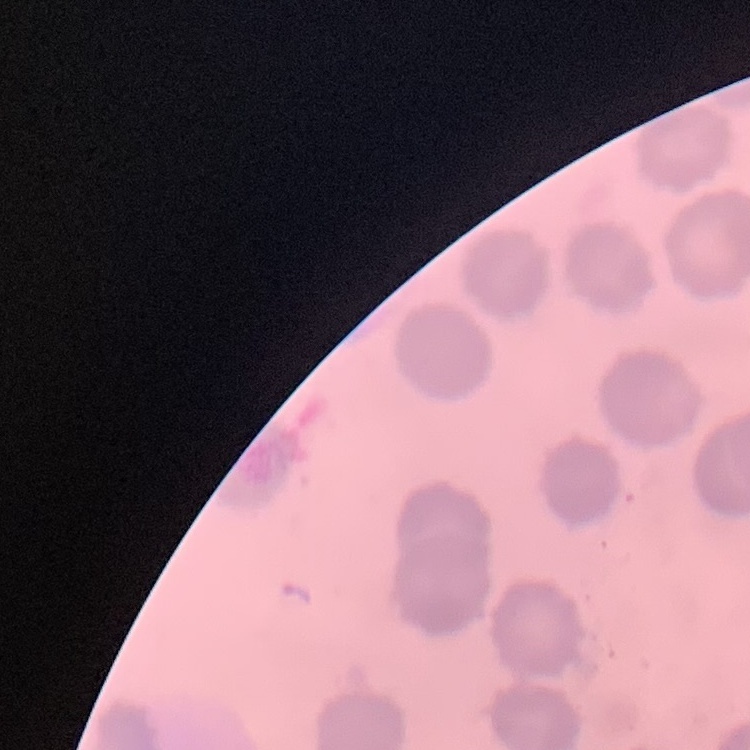

The erythrocytes exhibit no rouleaux formation. Field's or Giemsa stain. Thin blood smear. Square crop of a larger photomicrograph.